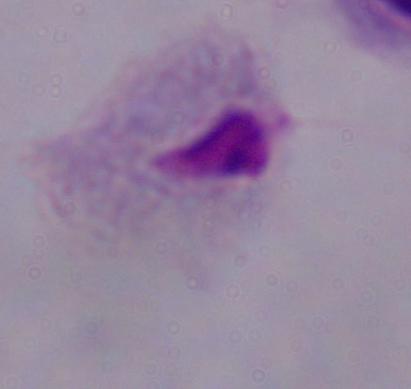

{
  "identification": "trichomonad",
  "magnification": "1000x",
  "modality": "micrograph"
}